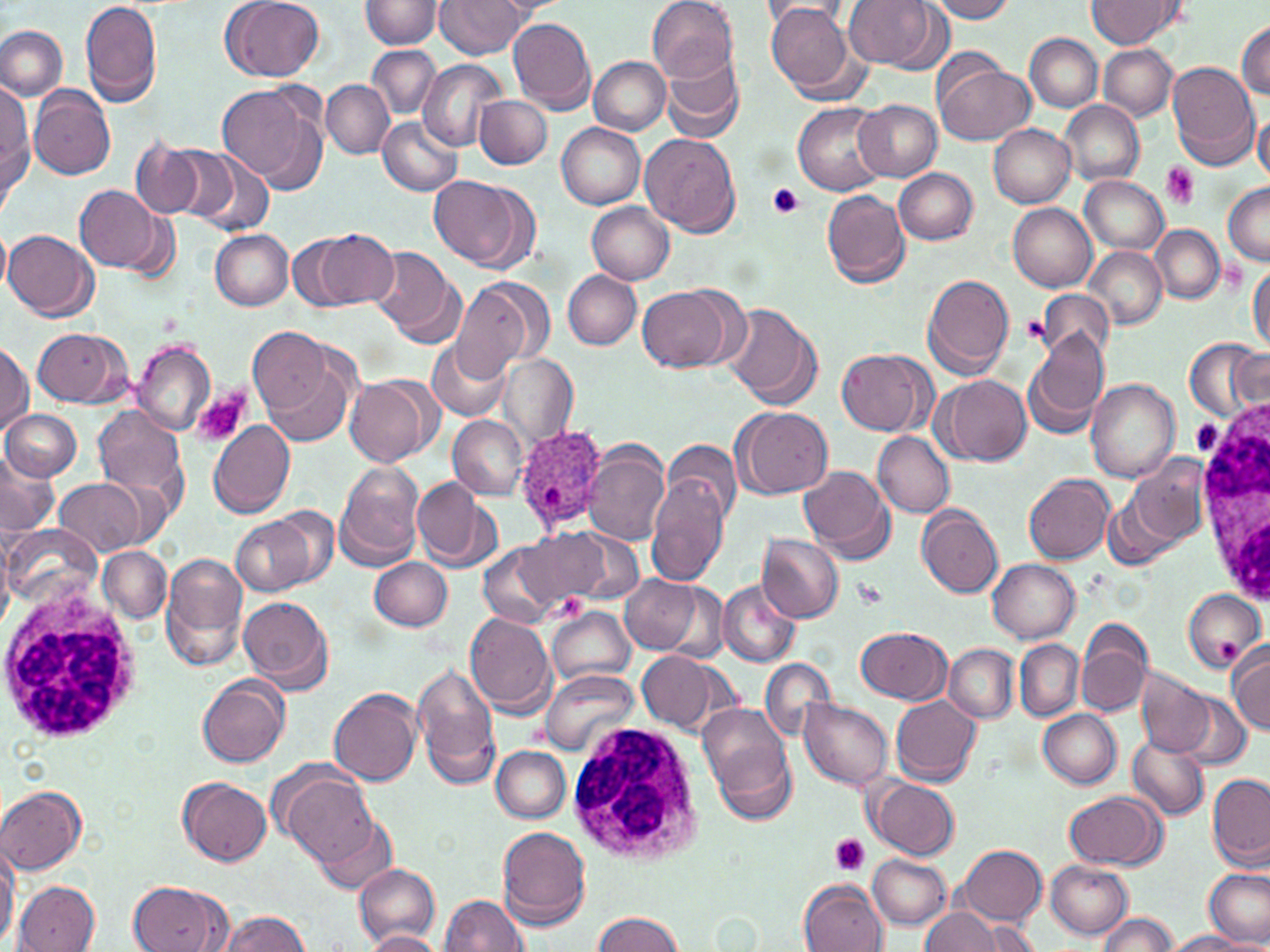

Approximate bounding boxes as named x1/y1/x2/y2 corners in pixels. White blood cell locations: (x1=1197, y1=390, x2=1270, y2=606), (x1=0, y1=581, x2=146, y2=746), (x1=567, y1=720, x2=704, y2=864). Plasmodium ovale-infected red blood cell locations: (x1=514, y1=426, x2=610, y2=533). Platelet locations: (x1=1161, y1=162, x2=1199, y2=208), (x1=768, y1=183, x2=803, y2=218), (x1=1022, y1=314, x2=1051, y2=347), (x1=193, y1=388, x2=250, y2=445), (x1=1192, y1=419, x2=1223, y2=455), (x1=853, y1=578, x2=888, y2=608), (x1=829, y1=835, x2=870, y2=875). Uninfected red blood cell locations: (x1=80, y1=0, x2=163, y2=109), (x1=221, y1=0, x2=325, y2=82), (x1=435, y1=0, x2=527, y2=57), (x1=491, y1=0, x2=568, y2=16), (x1=844, y1=0, x2=945, y2=71), (x1=927, y1=0, x2=1017, y2=23), (x1=1088, y1=0, x2=1179, y2=48), (x1=363, y1=1, x2=443, y2=49), (x1=647, y1=1, x2=738, y2=82), (x1=764, y1=1, x2=864, y2=102), (x1=507, y1=17, x2=595, y2=114), (x1=1236, y1=21, x2=1270, y2=98), (x1=0, y1=24, x2=68, y2=102), (x1=1025, y1=34, x2=1102, y2=112), (x1=368, y1=45, x2=440, y2=118), (x1=1098, y1=46, x2=1177, y2=120), (x1=662, y1=53, x2=745, y2=145), (x1=589, y1=56, x2=670, y2=135), (x1=932, y1=57, x2=1035, y2=147), (x1=417, y1=58, x2=506, y2=151), (x1=1166, y1=61, x2=1262, y2=170), (x1=321, y1=79, x2=394, y2=158), (x1=218, y1=82, x2=327, y2=193), (x1=1, y1=84, x2=33, y2=205), (x1=30, y1=86, x2=115, y2=181), (x1=474, y1=94, x2=552, y2=169), (x1=853, y1=99, x2=942, y2=180), (x1=1060, y1=101, x2=1144, y2=185), (x1=793, y1=102, x2=888, y2=196), (x1=1254, y1=111, x2=1270, y2=185), (x1=377, y1=115, x2=463, y2=197), (x1=555, y1=122, x2=646, y2=209), (x1=988, y1=123, x2=1075, y2=208), (x1=640, y1=132, x2=742, y2=237), (x1=131, y1=139, x2=205, y2=218), (x1=157, y1=145, x2=242, y2=227), (x1=188, y1=153, x2=278, y2=240), (x1=893, y1=167, x2=978, y2=245), (x1=429, y1=176, x2=539, y2=273), (x1=1079, y1=176, x2=1168, y2=256), (x1=1222, y1=182, x2=1270, y2=266), (x1=74, y1=184, x2=165, y2=274), (x1=820, y1=190, x2=910, y2=289), (x1=586, y1=202, x2=675, y2=285), (x1=1008, y1=204, x2=1097, y2=292), (x1=1150, y1=225, x2=1224, y2=303), (x1=0, y1=229, x2=11, y2=295), (x1=4, y1=229, x2=98, y2=322), (x1=211, y1=229, x2=292, y2=310), (x1=312, y1=229, x2=398, y2=308), (x1=288, y1=234, x2=363, y2=312), (x1=1083, y1=246, x2=1167, y2=331), (x1=371, y1=247, x2=462, y2=342), (x1=1248, y1=259, x2=1270, y2=353), (x1=562, y1=271, x2=641, y2=349), (x1=920, y1=273, x2=1017, y2=379), (x1=449, y1=277, x2=549, y2=380), (x1=636, y1=282, x2=744, y2=374), (x1=1037, y1=289, x2=1112, y2=368), (x1=723, y1=305, x2=821, y2=411), (x1=32, y1=327, x2=132, y2=407), (x1=247, y1=327, x2=333, y2=416), (x1=1023, y1=330, x2=1109, y2=438), (x1=427, y1=339, x2=512, y2=421), (x1=1186, y1=339, x2=1267, y2=423), (x1=128, y1=341, x2=216, y2=436), (x1=0, y1=342, x2=32, y2=434), (x1=837, y1=349, x2=931, y2=436), (x1=255, y1=351, x2=359, y2=448), (x1=497, y1=353, x2=578, y2=449), (x1=345, y1=375, x2=439, y2=468), (x1=933, y1=375, x2=1031, y2=467), (x1=1085, y1=379, x2=1182, y2=482), (x1=92, y1=406, x2=189, y2=508), (x1=734, y1=406, x2=834, y2=499), (x1=1, y1=409, x2=79, y2=481), (x1=447, y1=415, x2=527, y2=498), (x1=206, y1=420, x2=295, y2=518), (x1=873, y1=430, x2=954, y2=517), (x1=665, y1=440, x2=743, y2=524), (x1=582, y1=443, x2=672, y2=547), (x1=0, y1=450, x2=56, y2=540), (x1=1130, y1=454, x2=1213, y2=546), (x1=334, y1=462, x2=426, y2=572), (x1=801, y1=464, x2=895, y2=563), (x1=646, y1=469, x2=731, y2=585), (x1=1025, y1=473, x2=1114, y2=563), (x1=56, y1=478, x2=149, y2=558), (x1=410, y1=478, x2=499, y2=573), (x1=276, y1=506, x2=339, y2=587), (x1=917, y1=506, x2=1003, y2=598), (x1=231, y1=513, x2=321, y2=596), (x1=4, y1=523, x2=97, y2=610), (x1=519, y1=529, x2=613, y2=611), (x1=561, y1=530, x2=641, y2=606), (x1=756, y1=533, x2=845, y2=624), (x1=477, y1=540, x2=571, y2=629), (x1=98, y1=546, x2=171, y2=623), (x1=161, y1=554, x2=248, y2=671), (x1=368, y1=557, x2=453, y2=629), (x1=988, y1=560, x2=1081, y2=644), (x1=620, y1=576, x2=701, y2=652), (x1=718, y1=582, x2=801, y2=667), (x1=1183, y1=590, x2=1267, y2=671), (x1=237, y1=595, x2=333, y2=691), (x1=549, y1=609, x2=635, y2=684), (x1=464, y1=613, x2=555, y2=716), (x1=1076, y1=621, x2=1152, y2=718), (x1=856, y1=627, x2=951, y2=704), (x1=1014, y1=639, x2=1084, y2=720), (x1=1227, y1=642, x2=1270, y2=734), (x1=943, y1=645, x2=1018, y2=723), (x1=638, y1=650, x2=725, y2=734), (x1=758, y1=657, x2=836, y2=735), (x1=412, y1=662, x2=501, y2=787), (x1=1135, y1=667, x2=1216, y2=759), (x1=539, y1=671, x2=640, y2=755), (x1=197, y1=673, x2=291, y2=768), (x1=329, y1=687, x2=424, y2=786), (x1=1176, y1=694, x2=1254, y2=771), (x1=889, y1=695, x2=981, y2=784), (x1=798, y1=697, x2=894, y2=790), (x1=698, y1=704, x2=793, y2=800), (x1=1039, y1=709, x2=1122, y2=790), (x1=1126, y1=730, x2=1209, y2=822), (x1=709, y1=739, x2=796, y2=826), (x1=491, y1=746, x2=571, y2=823), (x1=278, y1=772, x2=377, y2=868), (x1=1207, y1=774, x2=1269, y2=864), (x1=177, y1=777, x2=272, y2=866), (x1=866, y1=779, x2=960, y2=860), (x1=1, y1=784, x2=87, y2=875), (x1=1064, y1=791, x2=1167, y2=870), (x1=312, y1=814, x2=398, y2=896), (x1=498, y1=826, x2=592, y2=930), (x1=0, y1=845, x2=19, y2=945), (x1=958, y1=845, x2=1048, y2=926), (x1=868, y1=856, x2=952, y2=929), (x1=1045, y1=860, x2=1133, y2=938), (x1=354, y1=864, x2=440, y2=946), (x1=1205, y1=868, x2=1270, y2=947), (x1=126, y1=878, x2=232, y2=952), (x1=799, y1=878, x2=888, y2=952), (x1=13, y1=881, x2=101, y2=951), (x1=439, y1=893, x2=528, y2=950), (x1=921, y1=907, x2=1001, y2=952), (x1=215, y1=911, x2=312, y2=950), (x1=593, y1=911, x2=686, y2=952), (x1=1096, y1=913, x2=1179, y2=951), (x1=978, y1=921, x2=1039, y2=952), (x1=362, y1=930, x2=444, y2=951), (x1=1166, y1=930, x2=1252, y2=951). Slide-level diagnosis: Plasmodium ovale. One field of a larger specimen. Thin blood smear. Captured at 1000x magnification. Image is 1270×952 pixels. May-Grünwald-Giemsa stain. Light microscopy.